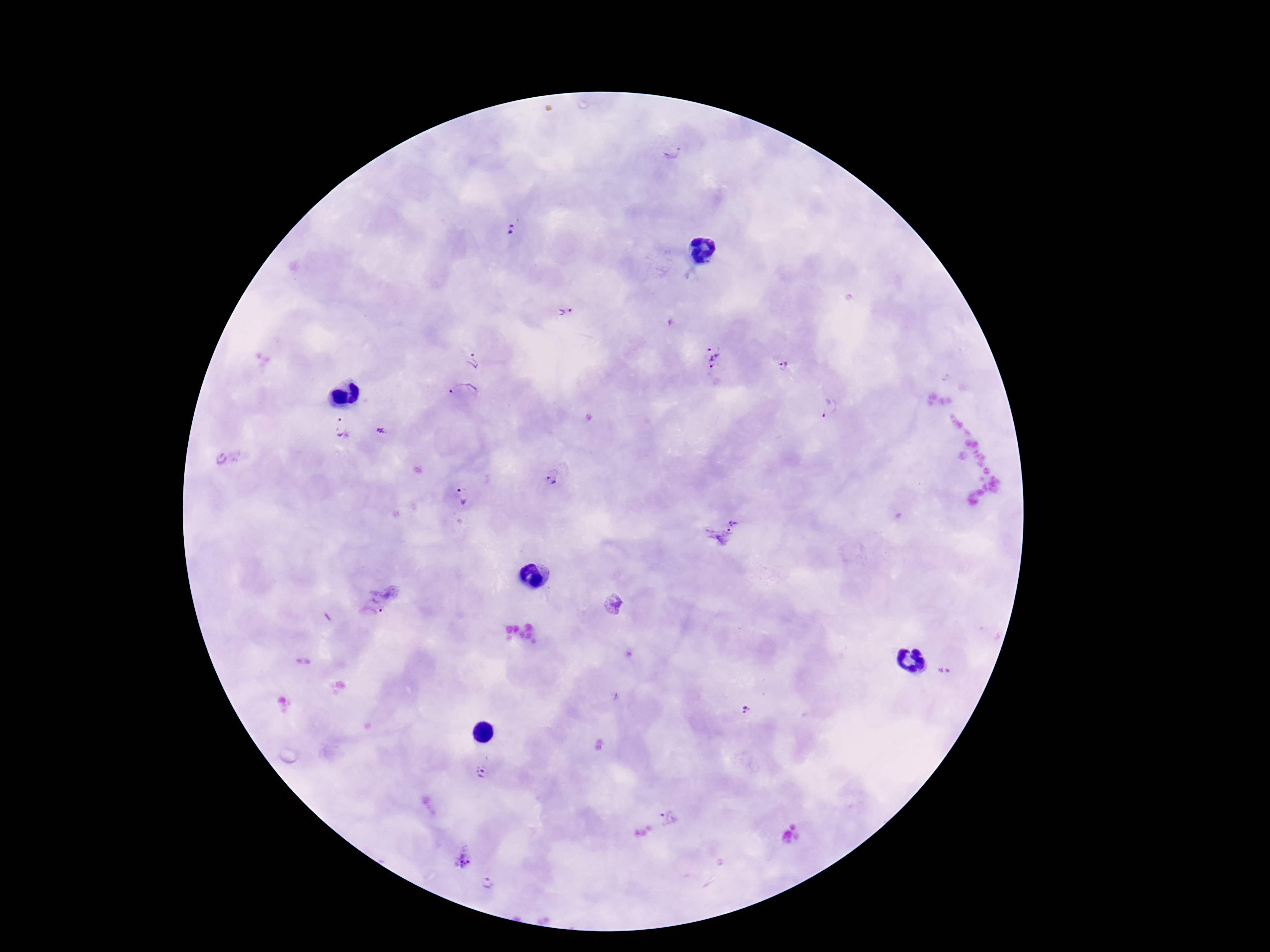
Approximate centers as [x, y] in pixels.
Summary:
  - Plasmodium parasite locations: [671, 145], [513, 230], [565, 313], [714, 355], [472, 362], [783, 366], [465, 398], [830, 407], [340, 427], [381, 430], [553, 478], [462, 496], [724, 530], [614, 606], [369, 610], [947, 670], [745, 709], [482, 772], [671, 817], [462, 858], [490, 883]
  - Stain: Giemsa
  - Field of view: one from this slide
  - Preparation: thick blood film
  - Image size: 1270×952 pixels
  - Magnification: 100x
  - Patient malaria status: positive
  - Capture: smartphone camera through the microscope eyepiece